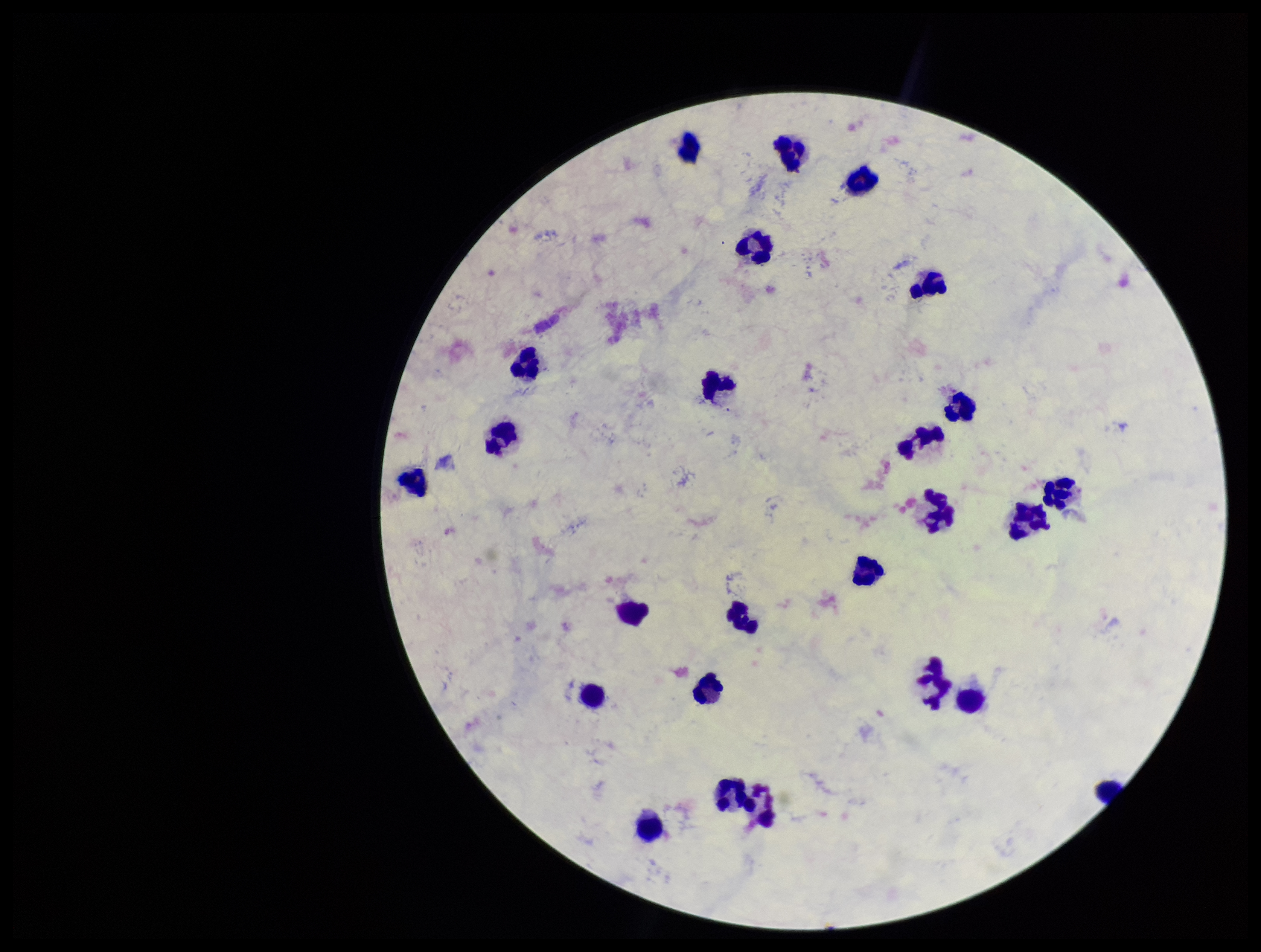

field of view = one from this slide
patient malaria status = negative
stain = Giemsa
Plasmodium parasites = none seen
parasite count = 0
image size = 1261×952 pixels
preparation = thick smear
leukocyte count = 24
capture = smartphone photograph through the microscope eyepiece